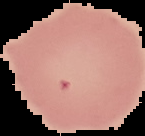

Summary:
  - Image type: segmented cell region on a black background
  - Image size: 145×136 pixels
  - Malaria status: uninfected
  - Preparation: thin blood smear